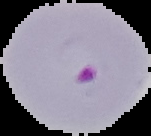

image size = 151×136 pixels
result = malaria parasites identified
image type = segmented cell region with the area outside set to black
preparation = thin blood film